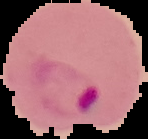
Summary:
  - Image type: segmented cell region on a black background
  - Malaria status: parasitized
  - Preparation: thin blood film
  - Image size: 148×139 pixels